Give the position of every Plasmodium parasite.
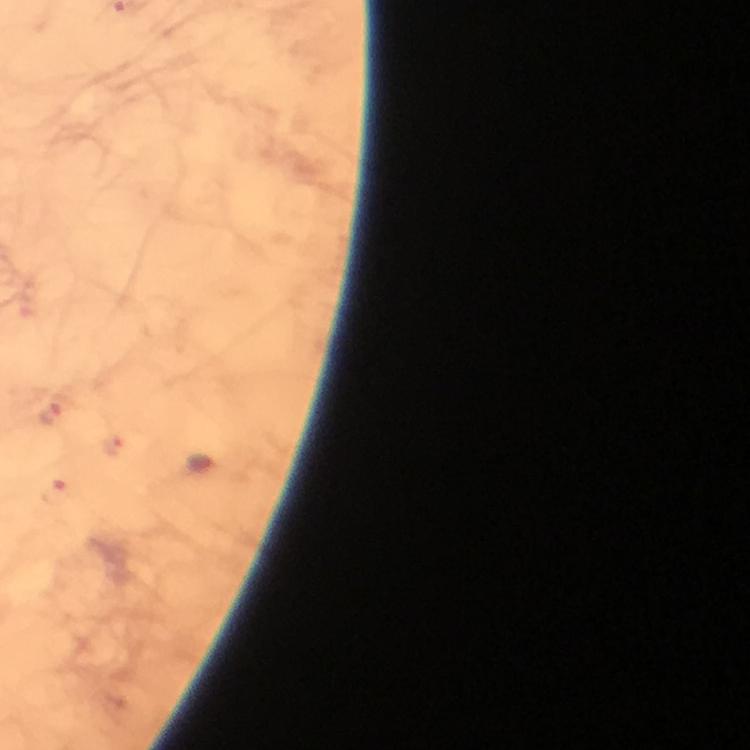

Approximate centers as [x, y] in pixels.
Plasmodium parasites: [54, 414], [113, 446], [59, 491].

A crop from one field of view. Image is 750×750 pixels. Photographed with a smartphone mounted on the microscope. Immersion oil was used. Giemsa-stained preparation. 100x magnification. Thick smear. From a malaria diagnostic workup.